Classify this cell by malaria status.
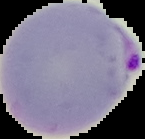

It is parasitized.

Summary:
  - Preparation: thin blood film
  - Image type: segmented cell region with the area outside set to black
  - Image size: 145×139 pixels